Identify the preparation type.
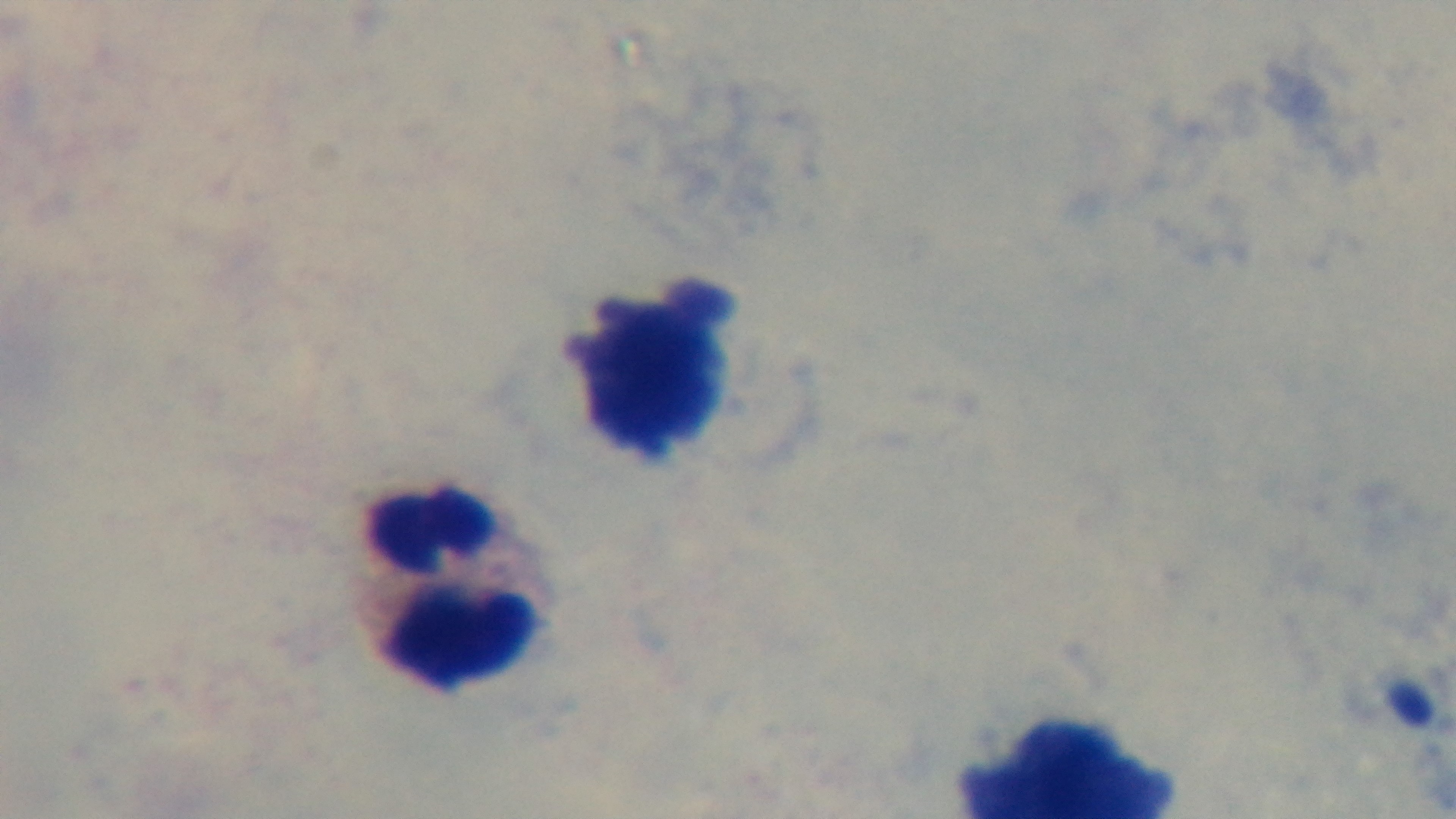

Thick.

Summary:
  - Capture: mounted 4K digital camera
  - Modality: light microscopy
  - Field of view: one from the slide
  - Malaria status: negative
  - Stain: Giemsa
  - Objective: 100x oil immersion